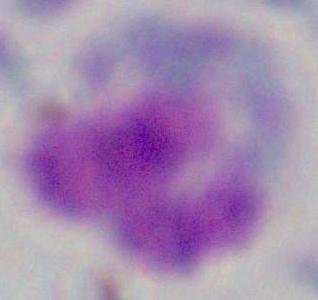

Summary:
  - Magnification: 1000x
  - Modality: photomicrograph
  - Identification: leukocyte